Assess this cell for malaria.
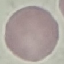
Uninfected.

preparation = thin blood film
stain = Giemsa
capture = smartphone camera at the microscope eyepiece
image type = cell patch, automatically extracted from a larger field of view and resized to 64 × 64 pixels